Give the location of every parasitized red blood cell.
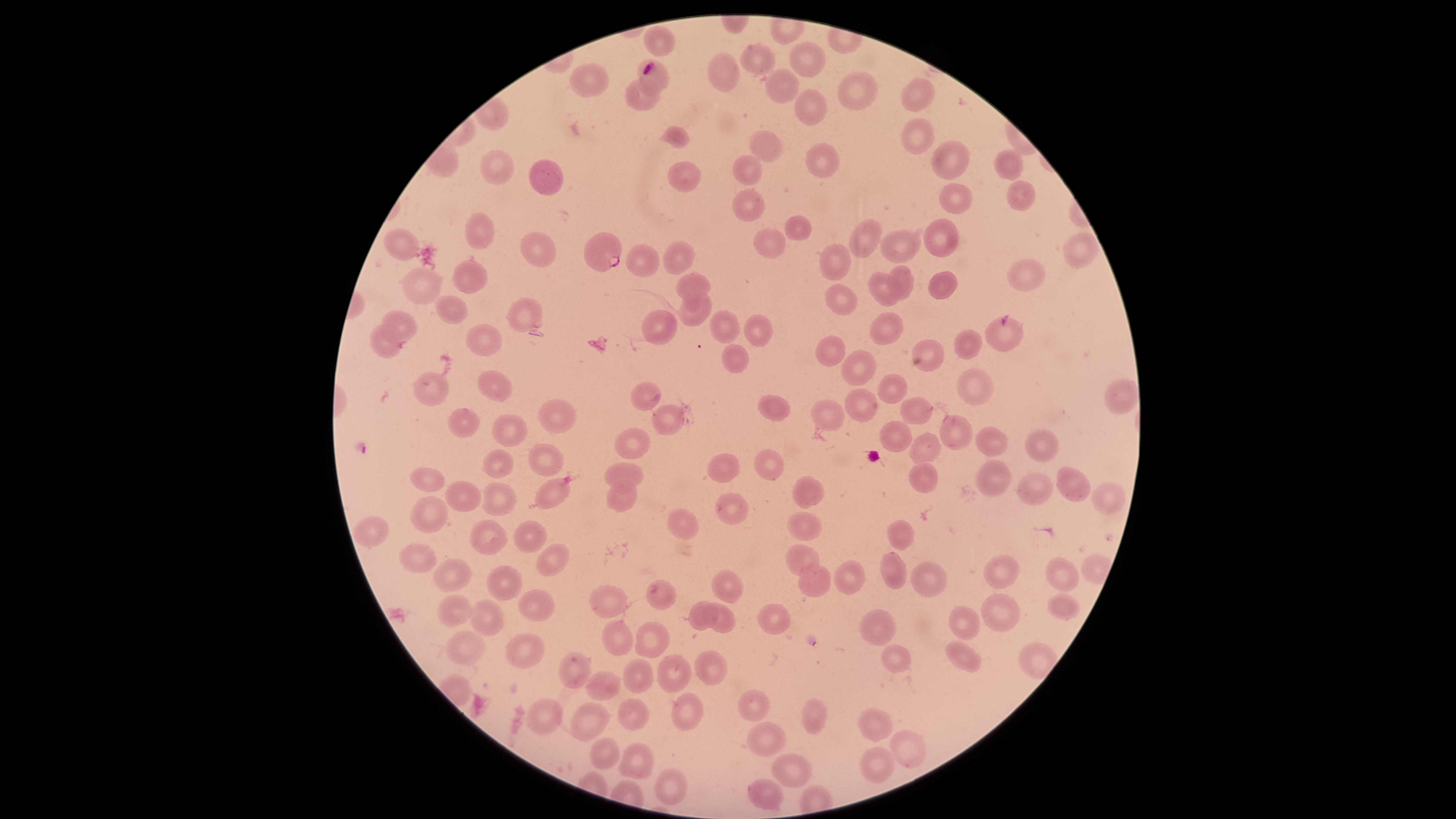

Approximate marker points, in pixels from the top-left corner.
Parasitized red blood cells: (x=598, y=248).

Approximate marker points, in pixels from the top-left corner.
Summary:
  - Uninfected red blood cells: (x=658, y=35), (x=752, y=54), (x=804, y=56), (x=721, y=72), (x=592, y=74), (x=655, y=74), (x=783, y=83), (x=853, y=87), (x=636, y=90), (x=923, y=90), (x=807, y=101), (x=676, y=133), (x=915, y=139), (x=762, y=142), (x=1000, y=157), (x=946, y=159), (x=826, y=160), (x=501, y=166), (x=750, y=168), (x=687, y=172), (x=548, y=174), (x=1018, y=195), (x=952, y=196), (x=752, y=205), (x=803, y=223), (x=483, y=232), (x=866, y=235), (x=935, y=238), (x=776, y=241), (x=906, y=242), (x=405, y=244), (x=1078, y=247), (x=540, y=255), (x=683, y=258), (x=834, y=259), (x=468, y=273), (x=1028, y=275), (x=695, y=278), (x=901, y=279), (x=428, y=284), (x=939, y=285), (x=881, y=294), (x=845, y=296), (x=449, y=305), (x=696, y=310), (x=525, y=311), (x=406, y=320), (x=756, y=324), (x=656, y=326), (x=727, y=326), (x=891, y=327), (x=995, y=331), (x=487, y=333), (x=966, y=343), (x=387, y=345), (x=827, y=353), (x=931, y=355), (x=735, y=359), (x=860, y=371), (x=492, y=381), (x=970, y=385), (x=899, y=387), (x=436, y=389), (x=645, y=392), (x=1117, y=395), (x=862, y=402), (x=776, y=403), (x=914, y=404), (x=828, y=407), (x=564, y=408), (x=657, y=412), (x=467, y=421), (x=508, y=422), (x=954, y=431), (x=891, y=434), (x=631, y=438), (x=992, y=440), (x=1049, y=441), (x=924, y=447), (x=546, y=456), (x=763, y=458), (x=503, y=462), (x=719, y=468), (x=922, y=472), (x=427, y=474), (x=621, y=474), (x=998, y=477), (x=1067, y=481), (x=1031, y=484), (x=461, y=489), (x=810, y=489), (x=552, y=494), (x=622, y=494), (x=501, y=496), (x=1103, y=496), (x=432, y=511), (x=734, y=511), (x=807, y=523), (x=685, y=526), (x=370, y=530), (x=901, y=534), (x=530, y=536), (x=484, y=539), (x=797, y=551), (x=418, y=556), (x=1090, y=563), (x=552, y=565), (x=1058, y=569), (x=459, y=570), (x=1009, y=572), (x=895, y=573), (x=844, y=578), (x=810, y=580), (x=929, y=580), (x=505, y=582), (x=732, y=585), (x=663, y=593), (x=611, y=603), (x=1064, y=606), (x=535, y=607), (x=1001, y=607), (x=463, y=610), (x=728, y=612), (x=486, y=616), (x=704, y=617), (x=767, y=621), (x=873, y=622), (x=972, y=623), (x=649, y=635), (x=621, y=639), (x=471, y=646), (x=893, y=652), (x=529, y=654), (x=960, y=656), (x=576, y=665), (x=667, y=665), (x=715, y=665), (x=638, y=673), (x=606, y=682), (x=752, y=696), (x=695, y=707), (x=552, y=709), (x=807, y=713), (x=642, y=716), (x=874, y=719), (x=599, y=720), (x=765, y=741), (x=605, y=748), (x=905, y=748), (x=638, y=760), (x=783, y=764), (x=875, y=768), (x=675, y=785), (x=763, y=788)
  - Capture: smartphone photograph through the microscope eyepiece
  - Species: Plasmodium falciparum
  - Stain: Giemsa
  - Preparation: thin smear of blood
  - Field of view: single
  - Image size: 1456×819 pixels
  - Visible region: circular